Give the position of every leukocyte visible.
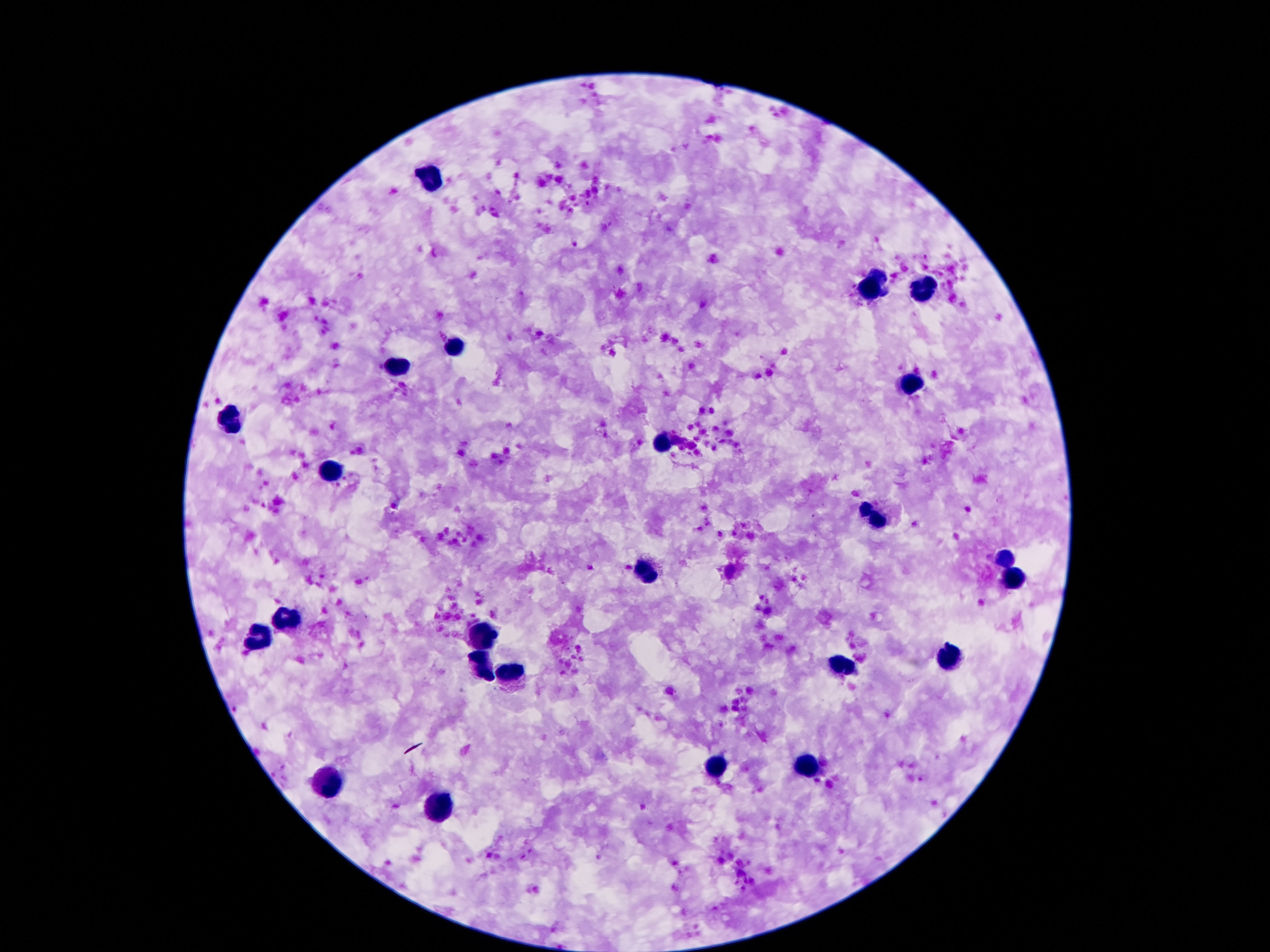
Approximate object centers, in pixels from the top-left corner.
Leukocytes: (x=428, y=180), (x=876, y=286), (x=921, y=290), (x=452, y=349), (x=400, y=367), (x=908, y=387), (x=230, y=419), (x=660, y=443), (x=331, y=475), (x=872, y=518), (x=1005, y=561), (x=648, y=572), (x=1009, y=579), (x=284, y=618), (x=482, y=636), (x=258, y=641), (x=945, y=660), (x=839, y=665), (x=482, y=669), (x=512, y=671), (x=717, y=769), (x=805, y=770), (x=325, y=789), (x=437, y=807).

Summary:
  - Image size: 1270×952 pixels
  - Field of view: one from this slide
  - Magnification: 100x
  - Capture: smartphone camera through the microscope eyepiece
  - Preparation: thick blood film
  - Stain: Giemsa
  - Patient malaria status: not infected